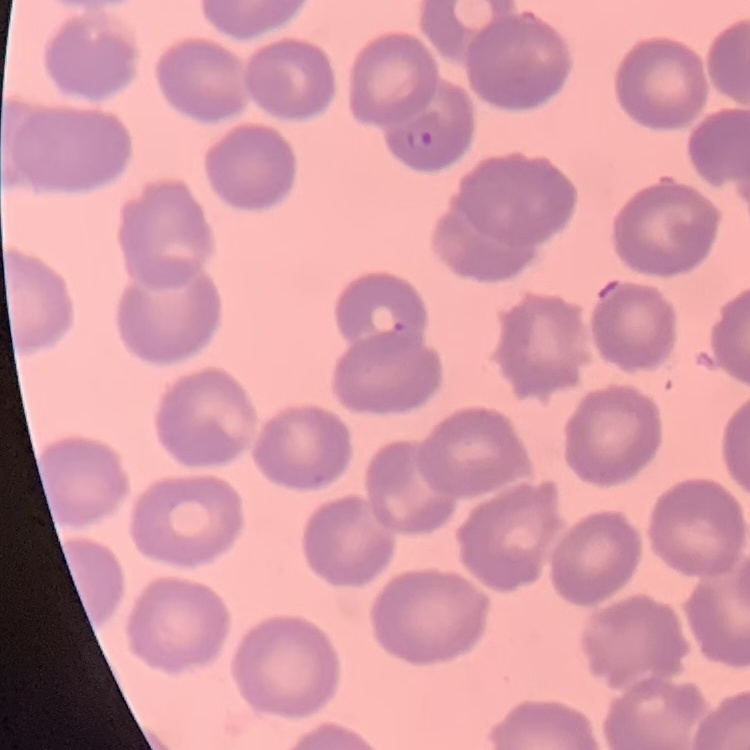

Summary:
  - Red blood cell morphology: no rouleaux formation
  - Stain: Field's or Giemsa
  - Image type: one tile cut from a larger photomicrograph
  - Preparation: thin peripheral smear